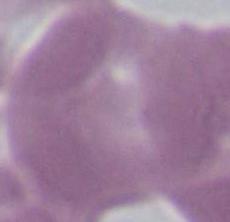

Summary:
  - Magnification: 1000x
  - Modality: photomicrograph
  - Identification: red blood cell